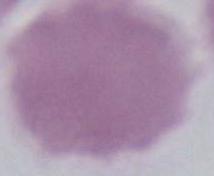
Summary:
  - Identification: erythrocyte
  - Modality: photomicrograph
  - Magnification: 1000x